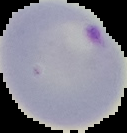

Image is 127×133 pixels. Segmented cell region on a black background. Malaria status: parasitized. From a thin blood film.